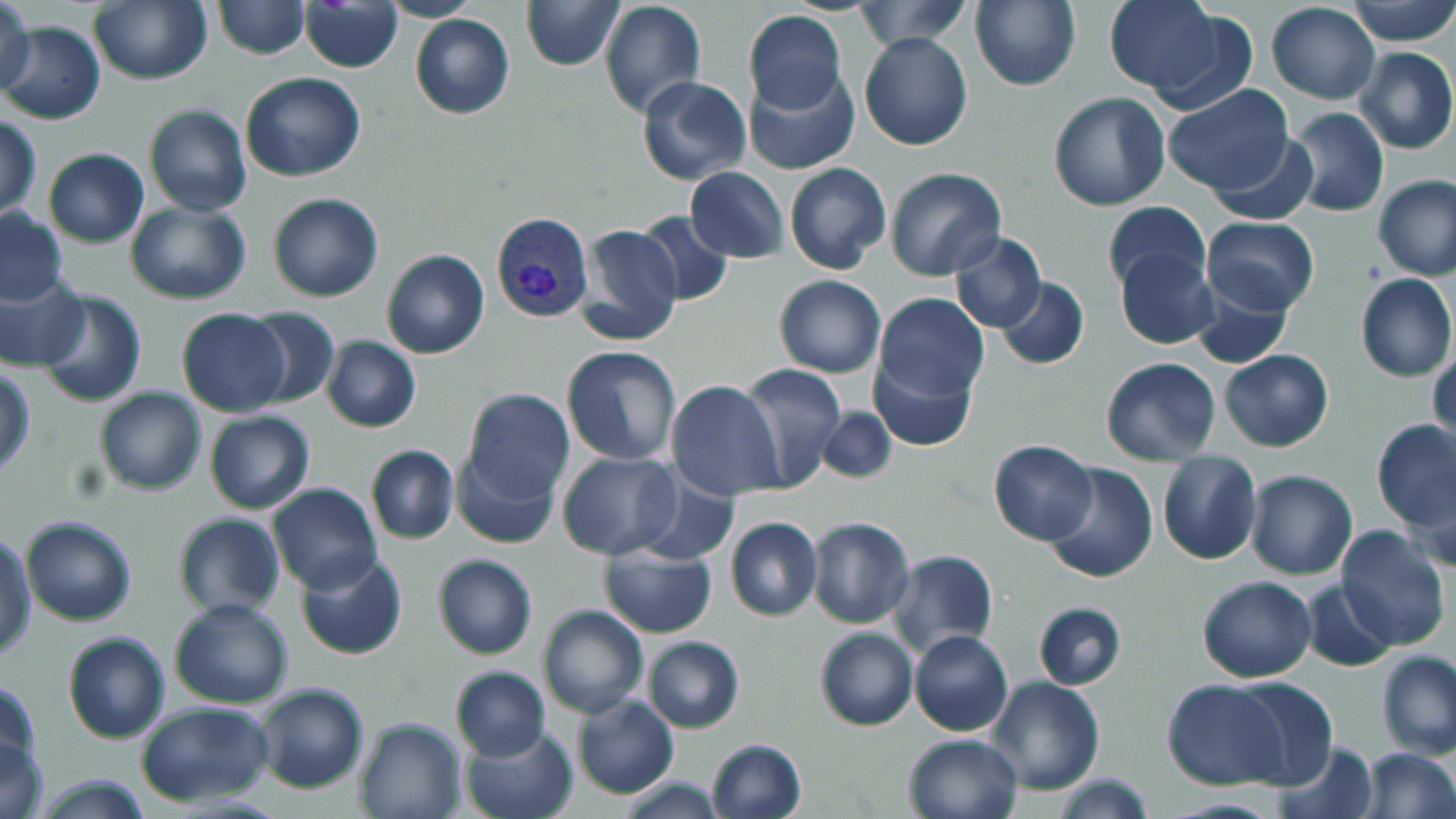
Approximate bounding boxes as named x1/y1/x2/y2 corners in pixels. Plasmodium vivax-infected red blood cell locations: (x1=491, y1=214, x2=594, y2=321). Uninfected red blood cell locations: (x1=2, y1=0, x2=37, y2=101), (x1=89, y1=0, x2=213, y2=85), (x1=521, y1=0, x2=624, y2=72), (x1=853, y1=0, x2=971, y2=52), (x1=972, y1=0, x2=1082, y2=92), (x1=1347, y1=0, x2=1456, y2=46), (x1=211, y1=1, x2=309, y2=59), (x1=1106, y1=1, x2=1224, y2=95), (x1=300, y1=2, x2=403, y2=72), (x1=599, y1=2, x2=707, y2=117), (x1=1266, y1=2, x2=1379, y2=103), (x1=1142, y1=9, x2=1259, y2=118), (x1=743, y1=10, x2=849, y2=115), (x1=409, y1=14, x2=514, y2=120), (x1=0, y1=21, x2=104, y2=125), (x1=859, y1=31, x2=973, y2=150), (x1=1355, y1=45, x2=1455, y2=155), (x1=744, y1=68, x2=860, y2=176), (x1=240, y1=72, x2=365, y2=182), (x1=638, y1=76, x2=751, y2=186), (x1=1163, y1=84, x2=1296, y2=198), (x1=1047, y1=92, x2=1170, y2=211), (x1=143, y1=104, x2=252, y2=216), (x1=1288, y1=107, x2=1389, y2=217), (x1=0, y1=116, x2=41, y2=218), (x1=1209, y1=132, x2=1314, y2=228), (x1=43, y1=148, x2=148, y2=248), (x1=785, y1=163, x2=892, y2=275), (x1=685, y1=167, x2=788, y2=263), (x1=883, y1=167, x2=1006, y2=282), (x1=1374, y1=176, x2=1456, y2=282), (x1=267, y1=193, x2=383, y2=302), (x1=126, y1=201, x2=252, y2=304), (x1=1101, y1=201, x2=1210, y2=294), (x1=0, y1=207, x2=69, y2=305), (x1=633, y1=212, x2=733, y2=307), (x1=1201, y1=217, x2=1319, y2=315), (x1=576, y1=225, x2=684, y2=346), (x1=948, y1=231, x2=1047, y2=333), (x1=381, y1=248, x2=489, y2=359), (x1=1117, y1=249, x2=1219, y2=347), (x1=0, y1=270, x2=91, y2=369), (x1=1355, y1=273, x2=1456, y2=383), (x1=774, y1=275, x2=886, y2=378), (x1=995, y1=277, x2=1090, y2=370), (x1=1191, y1=280, x2=1293, y2=368), (x1=33, y1=289, x2=148, y2=408), (x1=873, y1=292, x2=989, y2=406), (x1=177, y1=308, x2=289, y2=416), (x1=241, y1=308, x2=338, y2=410), (x1=320, y1=336, x2=421, y2=433), (x1=1429, y1=344, x2=1455, y2=446), (x1=561, y1=345, x2=682, y2=465), (x1=1220, y1=350, x2=1334, y2=453), (x1=869, y1=357, x2=978, y2=451), (x1=1099, y1=357, x2=1222, y2=467), (x1=735, y1=363, x2=847, y2=491), (x1=1, y1=367, x2=35, y2=475), (x1=664, y1=381, x2=783, y2=503), (x1=94, y1=386, x2=207, y2=497), (x1=459, y1=388, x2=578, y2=507), (x1=817, y1=405, x2=897, y2=483), (x1=205, y1=409, x2=314, y2=513), (x1=1373, y1=420, x2=1455, y2=531), (x1=987, y1=439, x2=1098, y2=546), (x1=452, y1=440, x2=563, y2=551), (x1=365, y1=445, x2=459, y2=545), (x1=557, y1=450, x2=682, y2=560), (x1=1157, y1=450, x2=1262, y2=566), (x1=1044, y1=464, x2=1159, y2=584), (x1=1246, y1=470, x2=1359, y2=580), (x1=635, y1=472, x2=743, y2=567), (x1=1408, y1=473, x2=1455, y2=571), (x1=265, y1=483, x2=383, y2=593), (x1=172, y1=512, x2=285, y2=621), (x1=21, y1=515, x2=135, y2=625), (x1=805, y1=516, x2=915, y2=629), (x1=725, y1=517, x2=822, y2=622), (x1=1335, y1=526, x2=1451, y2=649), (x1=0, y1=535, x2=36, y2=661), (x1=600, y1=544, x2=716, y2=639), (x1=295, y1=549, x2=407, y2=660), (x1=886, y1=549, x2=999, y2=661), (x1=433, y1=554, x2=538, y2=660), (x1=1195, y1=574, x2=1317, y2=683), (x1=1300, y1=581, x2=1398, y2=670), (x1=170, y1=598, x2=292, y2=709), (x1=1033, y1=600, x2=1127, y2=690), (x1=537, y1=603, x2=648, y2=719), (x1=814, y1=627, x2=919, y2=731), (x1=908, y1=629, x2=1014, y2=736), (x1=63, y1=633, x2=169, y2=743), (x1=642, y1=635, x2=744, y2=733), (x1=1377, y1=649, x2=1455, y2=761), (x1=449, y1=666, x2=550, y2=760), (x1=985, y1=674, x2=1105, y2=795), (x1=1227, y1=675, x2=1338, y2=787), (x1=1, y1=677, x2=41, y2=775), (x1=1162, y1=679, x2=1285, y2=790), (x1=252, y1=681, x2=369, y2=794), (x1=572, y1=694, x2=679, y2=799), (x1=136, y1=700, x2=274, y2=806), (x1=354, y1=715, x2=467, y2=819), (x1=461, y1=725, x2=580, y2=819), (x1=903, y1=732, x2=1022, y2=818), (x1=1, y1=735, x2=48, y2=818), (x1=705, y1=737, x2=807, y2=819), (x1=1277, y1=740, x2=1377, y2=818), (x1=1356, y1=748, x2=1456, y2=819), (x1=27, y1=773, x2=158, y2=817), (x1=1050, y1=773, x2=1158, y2=818), (x1=617, y1=777, x2=724, y2=817). Slide-level diagnosis: Plasmodium vivax. Image is 1456×819 pixels. Thin blood film. One field of a larger specimen. Light microscopy. Captured at 1000x magnification. May-Grünwald-Giemsa stain.